Assess the morphology of the erythrocytes.
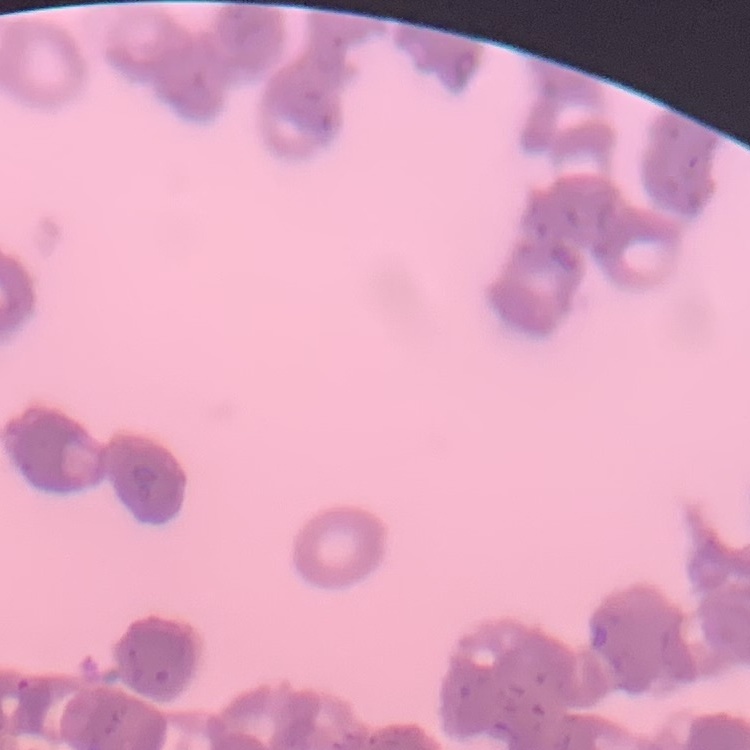

Rouleaux formation.

Summary:
  - Stain: Field's or Giemsa
  - Image type: square crop of a larger photomicrograph
  - Preparation: thin blood film